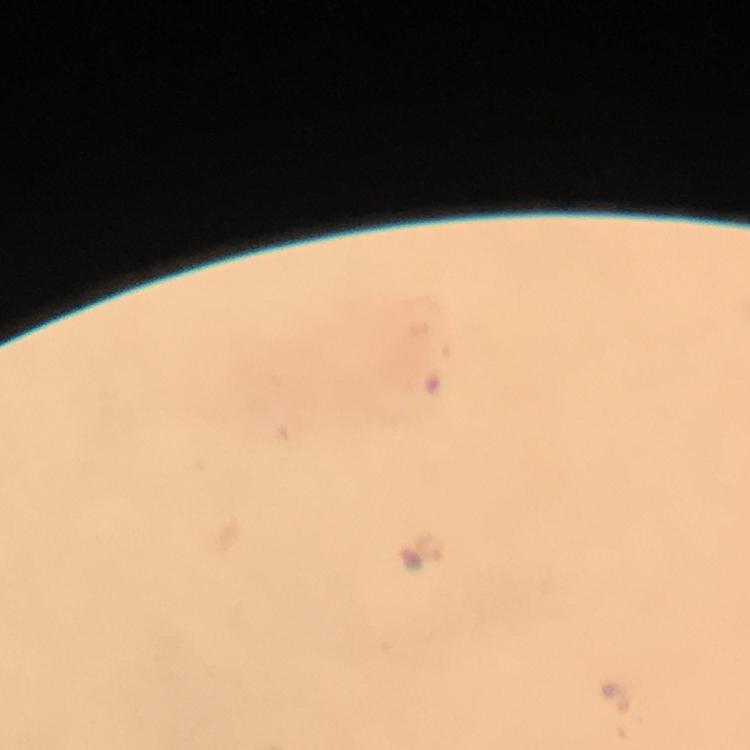

Approximate centers as (x, y) in pixels.
Summary:
  - Malaria parasite locations: (430, 549)
  - Capture: smartphone photograph through a microscope
  - Preparation: thick smear
  - Cropped from: one field of view
  - Stain: Giemsa
  - Context: from a diagnostic examination for malaria
  - Magnification: 100x
  - Immersion oil: used
  - Image size: 750×750 pixels